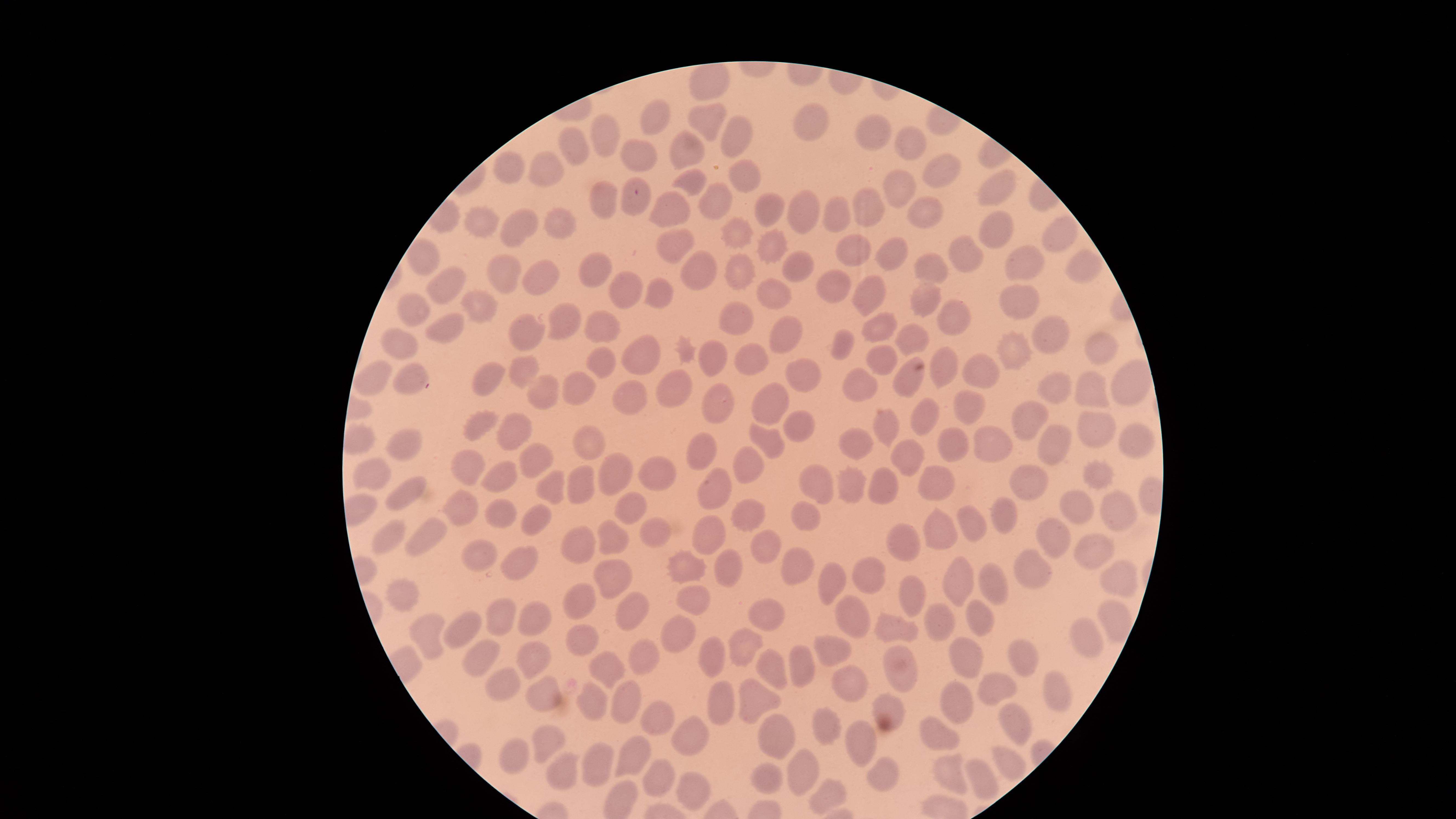
presence = no malaria parasites identified
preparation = thin blood smear
field of view = single
capture = smartphone photograph through the microscope eyepiece
image size = 1456×819 pixels
uninfected RBCs = approximate marker points as (x, y) in pixels: (653, 114), (706, 114), (813, 124), (874, 124), (738, 132), (912, 136), (601, 139), (689, 144), (572, 150), (641, 156), (548, 167), (509, 168), (943, 173), (739, 175), (695, 181), (896, 184), (992, 189), (608, 199), (716, 199), (635, 205), (766, 205), (863, 205), (801, 206), (676, 207), (924, 209), (840, 215), (515, 225), (485, 226), (554, 226), (735, 230), (995, 234), (1063, 235), (678, 242), (768, 243), (852, 248), (891, 253), (968, 254), (428, 259), (926, 262), (795, 263), (592, 265), (1017, 266), (1082, 266), (690, 267), (741, 272), (505, 274), (540, 274), (449, 284), (872, 285), (833, 287), (624, 292), (654, 294), (1018, 296), (778, 299), (481, 302), (924, 305), (412, 312), (570, 315), (947, 317), (731, 319), (875, 324), (448, 327), (1054, 327), (527, 330), (787, 331), (597, 333), (405, 343), (841, 343), (911, 343), (1101, 346), (638, 352), (714, 353), (1018, 353), (748, 358), (881, 364), (603, 365), (982, 366), (522, 369), (945, 371), (379, 372), (416, 373), (801, 373), (495, 375), (907, 377), (1127, 382), (673, 384), (862, 384), (545, 387), (579, 387), (1050, 387), (1096, 392), (719, 394), (632, 398), (964, 403), (771, 404), (927, 420), (1030, 420), (794, 423), (479, 425), (884, 425), (521, 426), (1099, 427), (980, 435), (1129, 437), (859, 439), (771, 440), (949, 441), (595, 443), (1052, 443), (403, 445), (538, 453), (706, 453), (905, 456), (750, 460), (467, 461), (617, 467), (377, 470), (502, 470), (649, 473), (1096, 474), (819, 478), (936, 478), (1025, 480), (717, 481), (546, 483), (581, 484), (881, 484), (852, 485), (404, 493), (461, 506), (1117, 506), (624, 507), (1085, 509), (503, 512), (752, 513), (809, 515), (1002, 515), (543, 521), (972, 524), (941, 528), (425, 532), (703, 532), (654, 533), (392, 534), (905, 536), (1055, 539), (579, 543), (614, 543), (1091, 543), (764, 544), (480, 549), (794, 559), (686, 562), (517, 564), (729, 568), (610, 572), (871, 573), (1026, 575), (832, 576), (993, 578), (1124, 578), (958, 584), (397, 593), (915, 595), (698, 597), (580, 598), (769, 608), (635, 610), (855, 610), (1109, 612), (505, 617), (531, 618), (981, 622), (936, 625), (459, 627), (896, 631), (428, 633), (580, 634), (678, 634), (1085, 635), (750, 644), (835, 649), (484, 650), (710, 652), (643, 653), (966, 656), (528, 661), (898, 661), (1019, 661), (769, 663), (799, 664), (605, 670), (496, 676), (849, 677), (1055, 688), (542, 689), (989, 689), (955, 699), (758, 700), (598, 702), (629, 702), (718, 703), (896, 707), (660, 714), (1017, 725), (822, 730), (943, 731), (696, 732), (552, 733), (778, 734), (860, 744), (520, 754), (626, 756), (598, 759), (1007, 760), (558, 766), (660, 769), (798, 769), (949, 773), (692, 774), (881, 776), (767, 778), (983, 779), (827, 792)
visible region = circular
stain = Giemsa